State the preparation type.
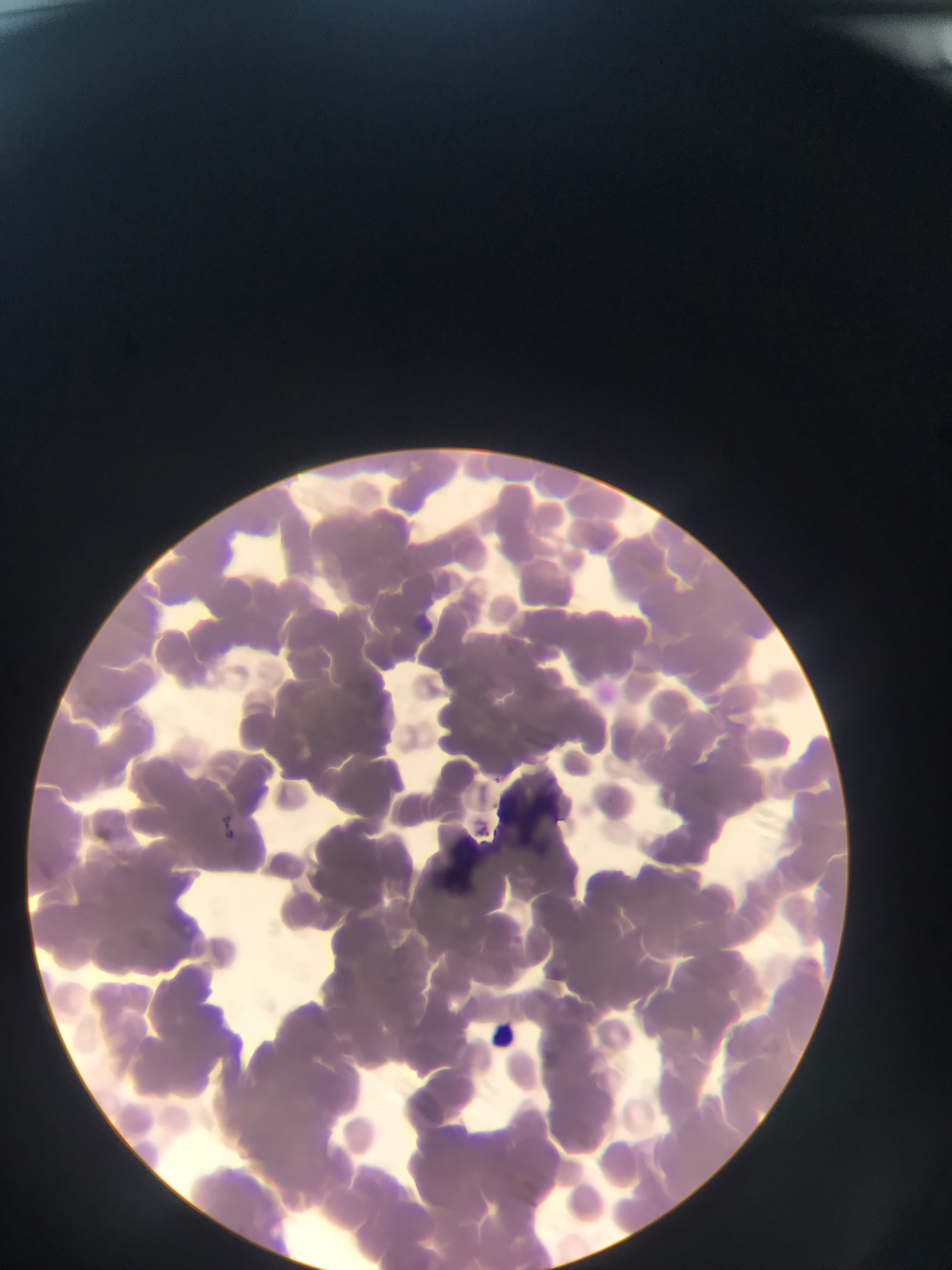
Thin blood smear.

{
  "leukocyte_locations": "approximate bounding boxes as left top right bottom in pixels: 484 1017 521 1053",
  "plasmodium_parasite_locations": "approximate bounding boxes as left top right bottom in pixels: 495 775 504 787",
  "field_of_view": "single",
  "image_size": "952×1270 pixels",
  "capture": "mobile-phone photograph through a microscope",
  "country": "Ghana"
}